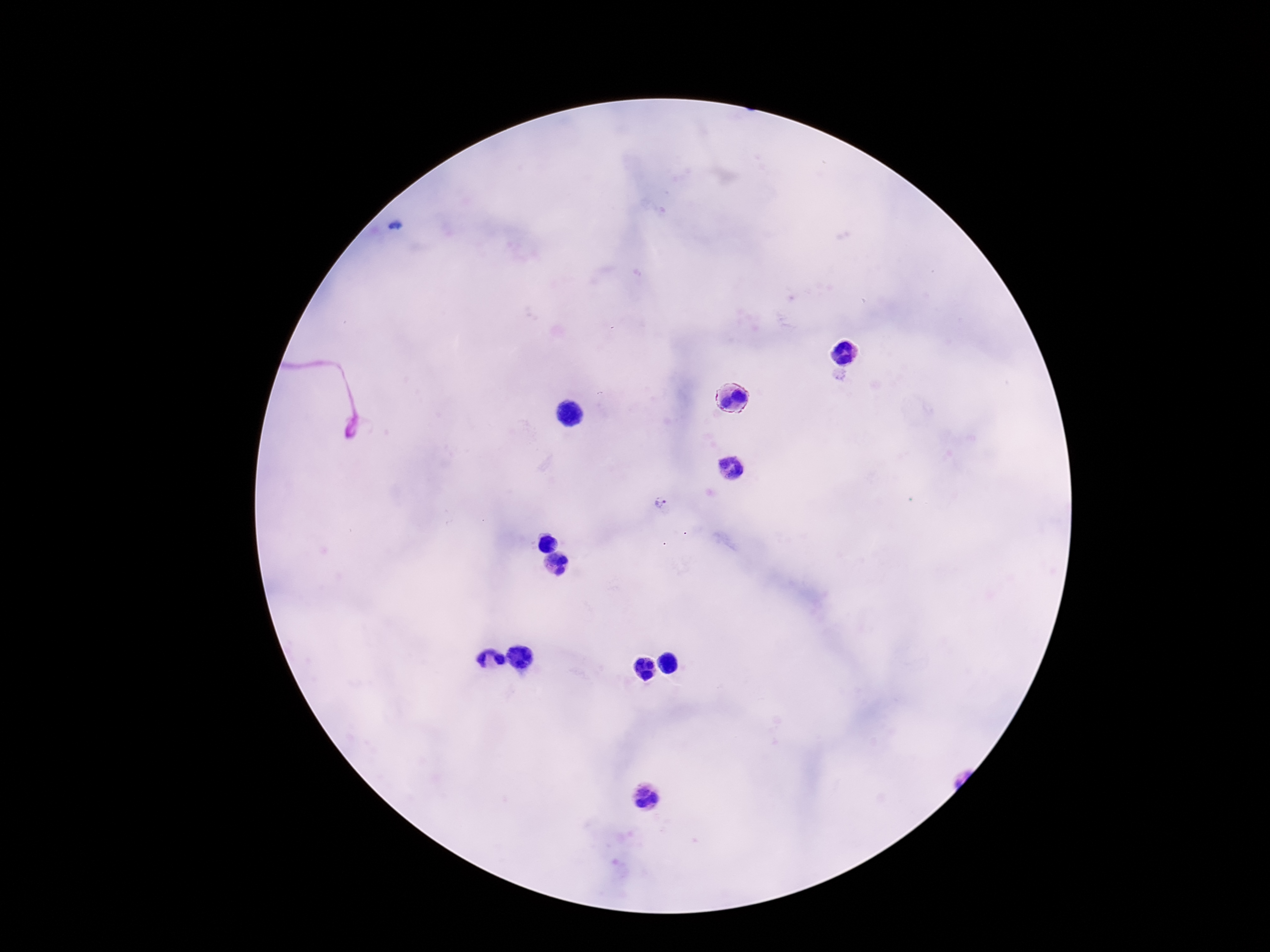

Approximate centers as [x, y] in pixels.
Summary:
  - Plasmodium parasite locations: [661, 504]
  - Capture: smartphone camera through the microscope eyepiece
  - Preparation: thick blood film
  - Image size: 1270×952 pixels
  - Stain: Giemsa
  - Field of view: one from this slide
  - Patient malaria status: positive
  - Magnification: 100x